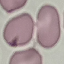
Result: no malaria parasites seen. Acquired by smartphone through the microscope eyepiece. Thin blood smear. Automatically extracted cell patch, resized to 64 × 64 pixels. Giemsa-stained preparation.